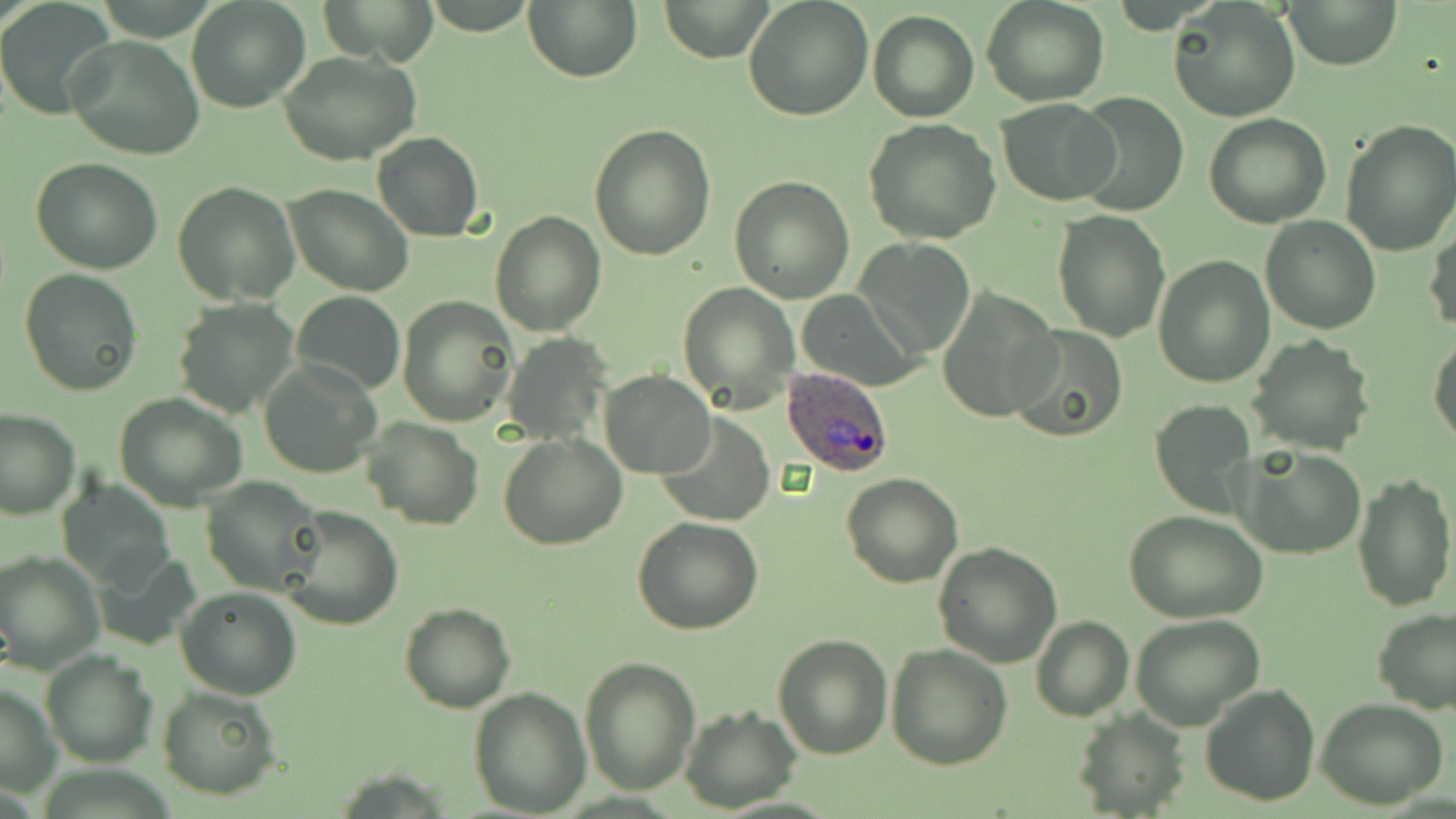 Approximate bounding boxes as named x1/y1/x2/y2 corners in pixels. Plasmodium ovale-infected red blood cell locations: (x1=780, y1=365, x2=896, y2=479). Uninfected red blood cell locations: (x1=185, y1=0, x2=310, y2=113), (x1=320, y1=0, x2=439, y2=66), (x1=524, y1=0, x2=642, y2=82), (x1=658, y1=0, x2=771, y2=62), (x1=743, y1=0, x2=873, y2=119), (x1=981, y1=0, x2=1110, y2=107), (x1=1282, y1=0, x2=1402, y2=70), (x1=1168, y1=1, x2=1301, y2=123), (x1=0, y1=5, x2=114, y2=120), (x1=867, y1=11, x2=979, y2=121), (x1=65, y1=36, x2=204, y2=160), (x1=281, y1=51, x2=422, y2=165), (x1=1074, y1=89, x2=1189, y2=217), (x1=998, y1=97, x2=1119, y2=204), (x1=1204, y1=112, x2=1331, y2=227), (x1=864, y1=119, x2=1003, y2=244), (x1=1339, y1=120, x2=1456, y2=257), (x1=588, y1=124, x2=715, y2=261), (x1=372, y1=132, x2=484, y2=242), (x1=30, y1=157, x2=163, y2=275), (x1=729, y1=175, x2=855, y2=303), (x1=173, y1=180, x2=300, y2=304), (x1=285, y1=184, x2=414, y2=296), (x1=490, y1=209, x2=605, y2=335), (x1=1052, y1=209, x2=1172, y2=342), (x1=1260, y1=216, x2=1380, y2=335), (x1=1426, y1=220, x2=1456, y2=337), (x1=858, y1=238, x2=976, y2=357), (x1=1153, y1=255, x2=1274, y2=388), (x1=19, y1=269, x2=143, y2=395), (x1=678, y1=282, x2=798, y2=412), (x1=937, y1=288, x2=1060, y2=423), (x1=291, y1=290, x2=405, y2=396), (x1=796, y1=290, x2=922, y2=391), (x1=399, y1=294, x2=519, y2=427), (x1=172, y1=298, x2=302, y2=419), (x1=1006, y1=326, x2=1129, y2=442), (x1=503, y1=333, x2=609, y2=445), (x1=1429, y1=333, x2=1456, y2=448), (x1=1246, y1=335, x2=1376, y2=455), (x1=260, y1=361, x2=380, y2=479), (x1=600, y1=369, x2=715, y2=478), (x1=114, y1=393, x2=248, y2=511), (x1=1150, y1=399, x2=1257, y2=517), (x1=0, y1=408, x2=80, y2=519), (x1=656, y1=412, x2=775, y2=526), (x1=364, y1=417, x2=485, y2=530), (x1=499, y1=433, x2=627, y2=550), (x1=1236, y1=446, x2=1366, y2=559), (x1=1351, y1=470, x2=1456, y2=613), (x1=842, y1=473, x2=963, y2=588), (x1=202, y1=476, x2=326, y2=595), (x1=60, y1=479, x2=177, y2=590), (x1=280, y1=506, x2=403, y2=630), (x1=1125, y1=511, x2=1268, y2=624), (x1=632, y1=518, x2=763, y2=636), (x1=933, y1=542, x2=1062, y2=665), (x1=0, y1=550, x2=104, y2=672), (x1=96, y1=552, x2=203, y2=649), (x1=176, y1=586, x2=302, y2=699), (x1=399, y1=602, x2=517, y2=713), (x1=1372, y1=608, x2=1455, y2=714), (x1=1130, y1=614, x2=1264, y2=731), (x1=1030, y1=617, x2=1133, y2=722), (x1=772, y1=632, x2=893, y2=758), (x1=886, y1=643, x2=1012, y2=770), (x1=42, y1=649, x2=156, y2=768), (x1=580, y1=655, x2=702, y2=796), (x1=1199, y1=683, x2=1323, y2=806), (x1=0, y1=684, x2=60, y2=799), (x1=157, y1=685, x2=282, y2=800), (x1=469, y1=687, x2=593, y2=815), (x1=1315, y1=698, x2=1448, y2=809), (x1=681, y1=707, x2=802, y2=811), (x1=1073, y1=708, x2=1189, y2=818). Slide-level diagnosis: Plasmodium ovale. Thin blood film. Captured at 1000x magnification. One field of a larger specimen. May-Grünwald-Giemsa-stained preparation. Optical microscopy. Image is 1456×819 pixels.